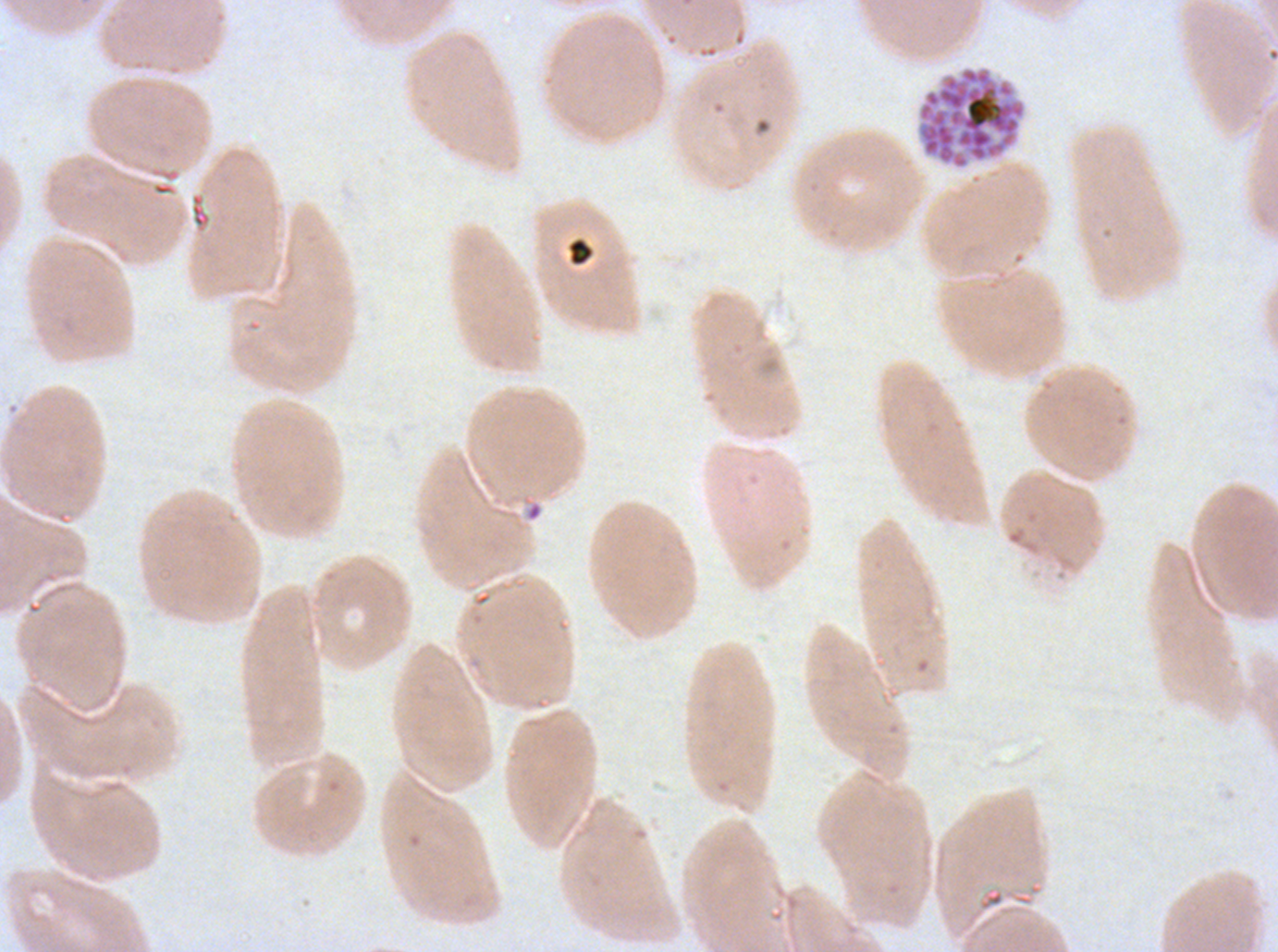 Approximate bounding boxes as {x1, y1, x2, y2} in pixels. Segmenter locations: {916, 66, 1026, 170}. Debris locations: {567, 238, 594, 266}. Image is 1278×952 pixels. P. falciparum cultured ex vivo for 24 to 48 hours, from a patient in The Gambia. One sub-image of a larger composite. Thin blood smear. Giemsa stain.